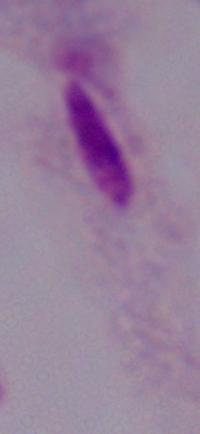

Summary:
  - Modality: photomicrograph
  - Magnification: 1000x
  - Identification: trichomonad